Which red blood cells are P. falciparum-infected, and which are of indeterminate infection status?
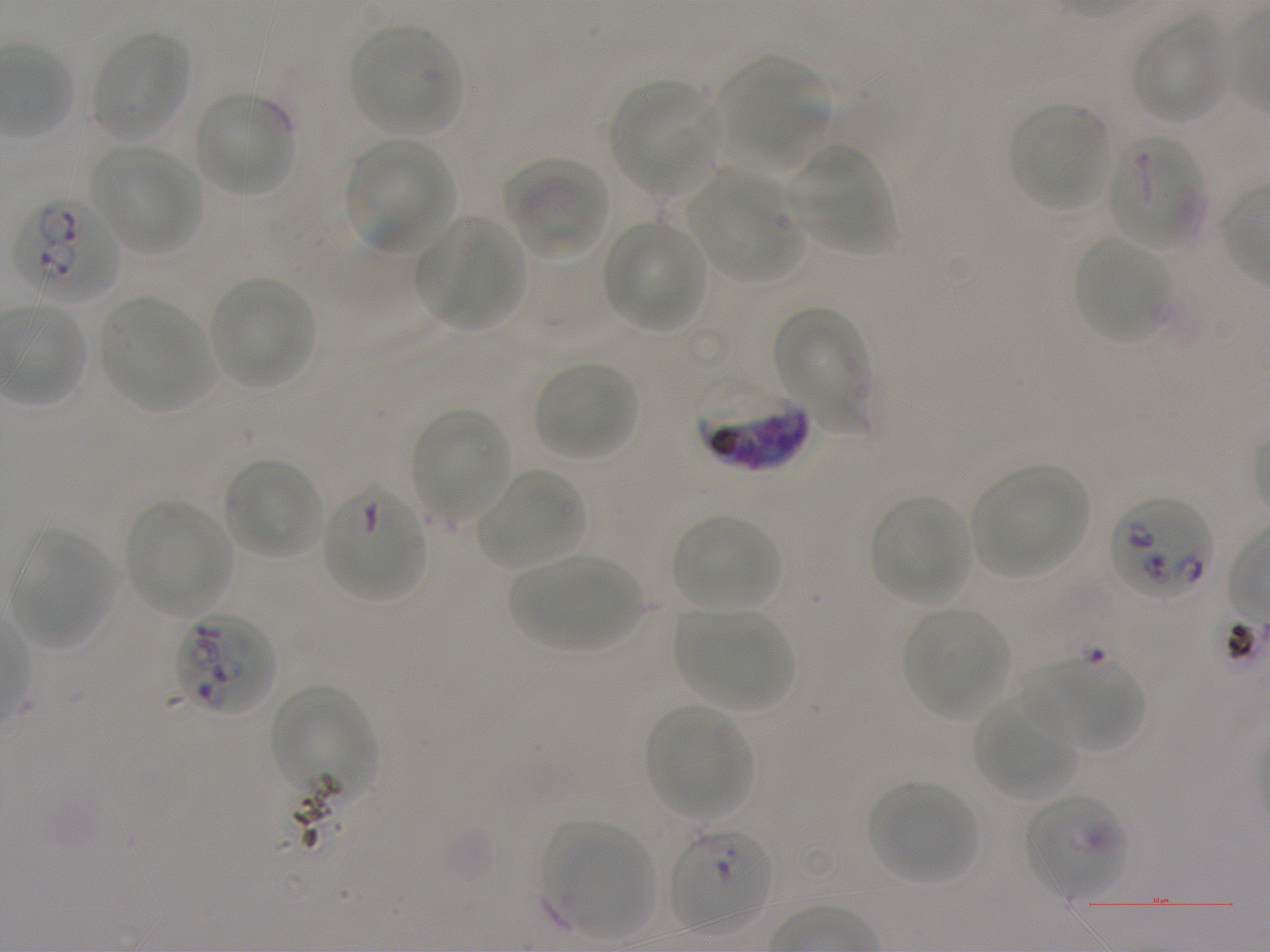
Approximate bounding rectangles given as corner coordinates in pixels from the top-left. Not every red blood cell is marked. A life-cycle stage — or a range of stages, where the recorded stages span more than one — follows each staged infected red blood cell.
Infected red blood cells: (x1=14, y1=196, x2=120, y2=303); (x1=695, y1=381, x2=807, y2=472); (x1=1109, y1=495, x2=1214, y2=599); (x1=177, y1=613, x2=275, y2=716); (x1=271, y1=685, x2=377, y2=799); (x1=669, y1=828, x2=772, y2=933) ring.
Red blood cells of indeterminate infection status: (x1=1107, y1=134, x2=1205, y2=249), (x1=322, y1=486, x2=427, y2=602), (x1=1023, y1=793, x2=1129, y2=900).

{
  "locations_of_uninfected_red_blood_cells": "(x1=1133, y1=15, x2=1228, y2=123), (x1=350, y1=23, x2=463, y2=135), (x1=90, y1=30, x2=192, y2=142), (x1=715, y1=56, x2=828, y2=170), (x1=609, y1=79, x2=713, y2=192), (x1=192, y1=91, x2=296, y2=197), (x1=1009, y1=103, x2=1111, y2=210), (x1=345, y1=139, x2=454, y2=255), (x1=786, y1=145, x2=895, y2=253), (x1=92, y1=146, x2=200, y2=255), (x1=507, y1=157, x2=610, y2=259), (x1=689, y1=172, x2=802, y2=281), (x1=415, y1=216, x2=524, y2=331), (x1=603, y1=220, x2=708, y2=333), (x1=1074, y1=235, x2=1170, y2=343), (x1=209, y1=277, x2=314, y2=388), (x1=99, y1=296, x2=214, y2=412), (x1=774, y1=306, x2=874, y2=432), (x1=532, y1=359, x2=638, y2=460), (x1=412, y1=410, x2=511, y2=522), (x1=222, y1=457, x2=322, y2=559), (x1=970, y1=466, x2=1090, y2=579), (x1=475, y1=469, x2=584, y2=569), (x1=869, y1=495, x2=971, y2=604), (x1=126, y1=499, x2=235, y2=618), (x1=671, y1=514, x2=781, y2=611), (x1=10, y1=531, x2=116, y2=650), (x1=508, y1=553, x2=642, y2=651), (x1=903, y1=607, x2=1012, y2=719), (x1=675, y1=608, x2=793, y2=711), (x1=1021, y1=659, x2=1143, y2=749), (x1=971, y1=696, x2=1078, y2=801), (x1=644, y1=704, x2=751, y2=818), (x1=867, y1=781, x2=979, y2=886), (x1=544, y1=821, x2=653, y2=940)",
  "image_size": "1270×952 pixels",
  "donor_blood_group": "A+",
  "culture": "in-vitro P. falciparum strain NF54, static",
  "preparation": "thin blood smear",
  "objective": "100x, oil immersion, numerical aperture 1.25",
  "stain": "Giemsa",
  "field_of_view": "one from this slide"
}